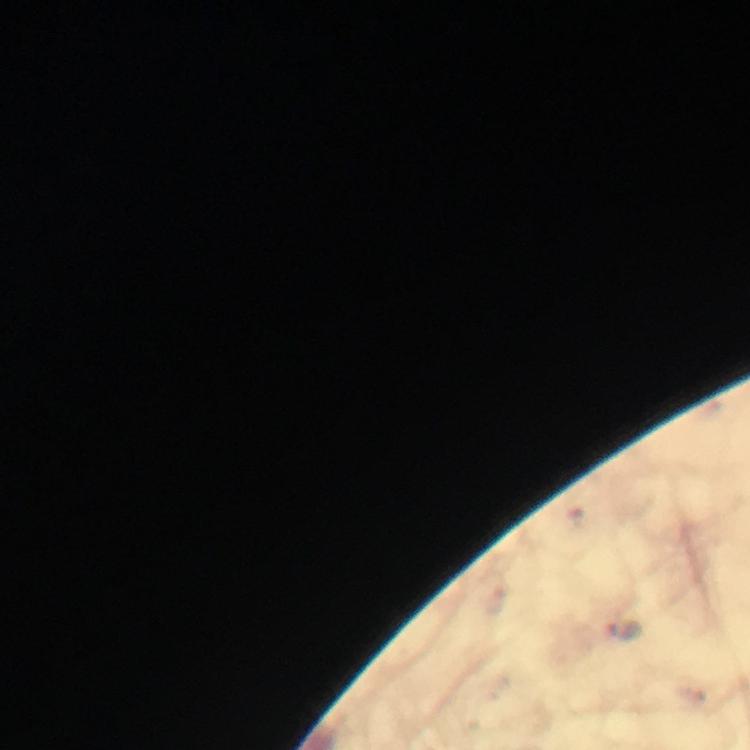
Approximate centers as (x, y) in pixels. Malaria parasite locations: (623, 630). Giemsa-stained preparation. Immersion oil applied. 100x magnification. From a malaria diagnostic workup. A crop from one field of view. Thick blood smear. Image is 750×750 pixels. Smartphone photograph taken through a microscope.